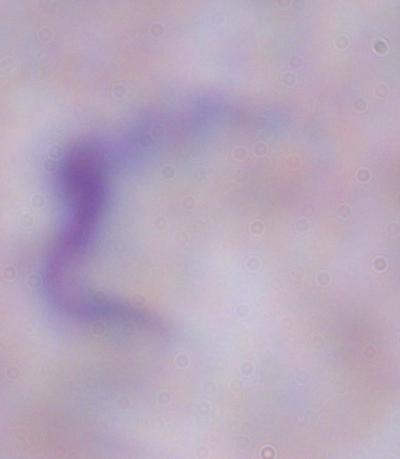
Captured at 1000x magnification. A trypanosome is shown. Photomicrograph.